Describe the morphology of the erythrocytes.
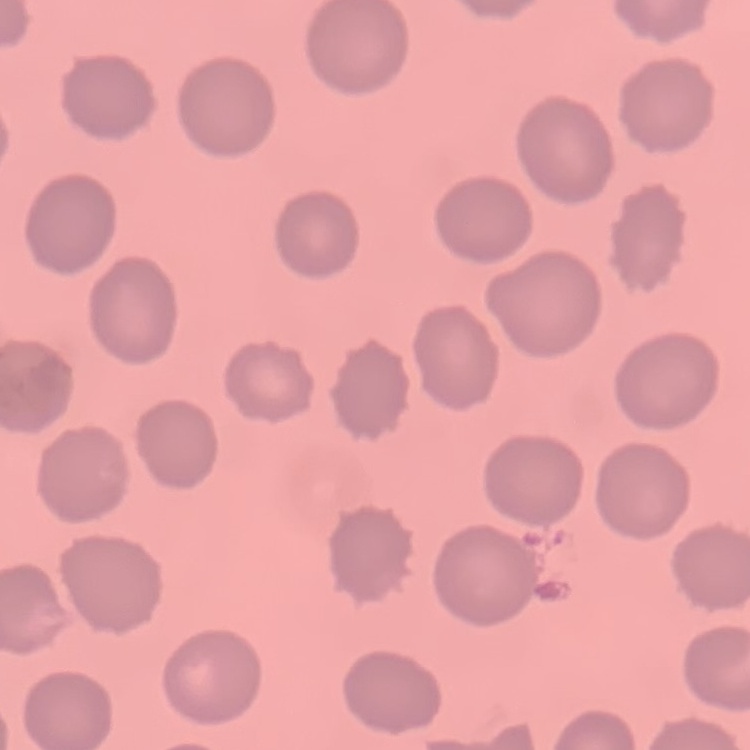

No rouleaux formation.

Field's or Giemsa stain. Thin peripheral smear. One tile cut from a larger photomicrograph.